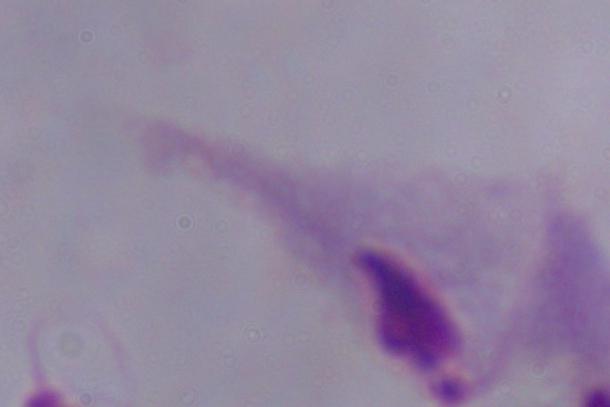 Captured at 1000x magnification. Micrograph. A trichomonad is shown.